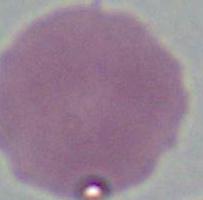

{
  "modality": "micrograph",
  "identification": "red blood cell",
  "magnification": "1000x"
}